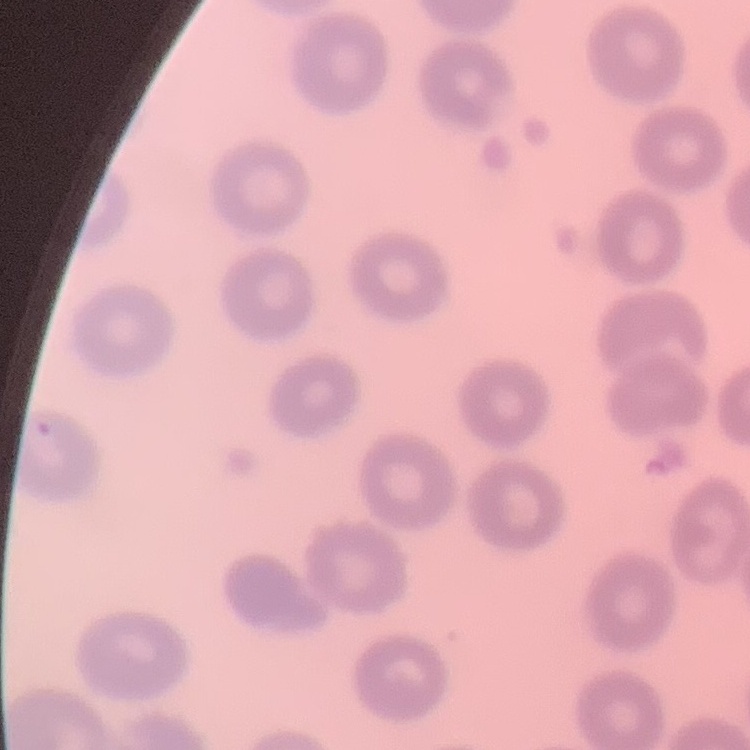
red_blood_cell_morphology: no rouleaux formation
image_type: square crop of a larger photomicrograph
stain: Field's or Giemsa
preparation: thin blood film